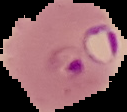
{
  "image_type": "cell region segmented out of the field of view; surrounding area masked to black",
  "preparation": "thin blood smear",
  "image_size": "127×112 pixels",
  "result": "malaria parasites detected"
}